Give the position of every leukocyte visible.
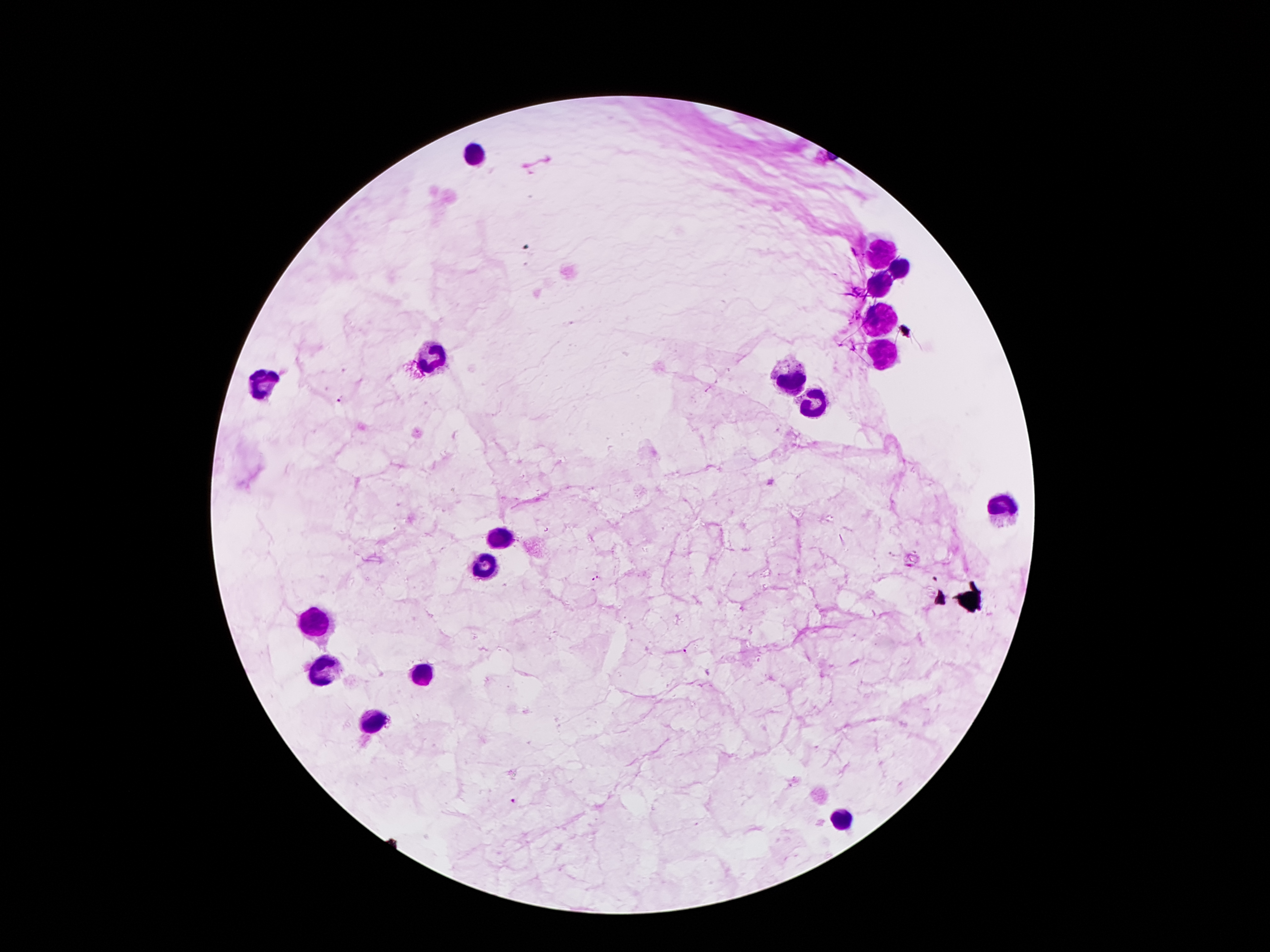

Approximate centers as {x, y} in pixels.
Leukocytes: {474, 154}, {879, 252}, {902, 269}, {879, 282}, {879, 320}, {881, 351}, {433, 355}, {790, 379}, {263, 385}, {816, 402}, {1004, 504}, {500, 540}, {487, 568}, {315, 616}, {323, 668}, {420, 674}, {373, 721}, {840, 820}.

Summary:
  - Malaria parasite locations: {341, 402}, {598, 576}, {591, 579}, {935, 579}, {685, 652}, {515, 802}
  - Magnification: 100x
  - Field of view: single
  - Image size: 1270×952 pixels
  - Patient malaria status: infected with Plasmodium falciparum
  - Capture: smartphone camera through the microscope eyepiece
  - Preparation: thick peripheral-blood smear
  - Stain: Giemsa